State which parasite is depicted.
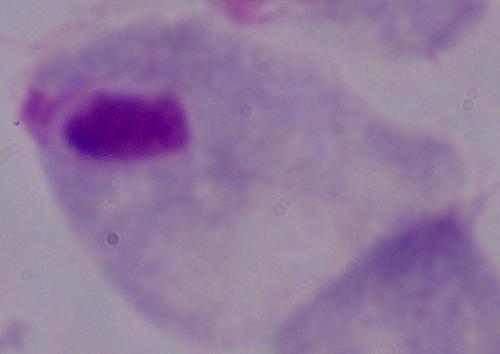
A trichomonad.

modality = photomicrograph
magnification = 1000x